Point out each leukocyte.
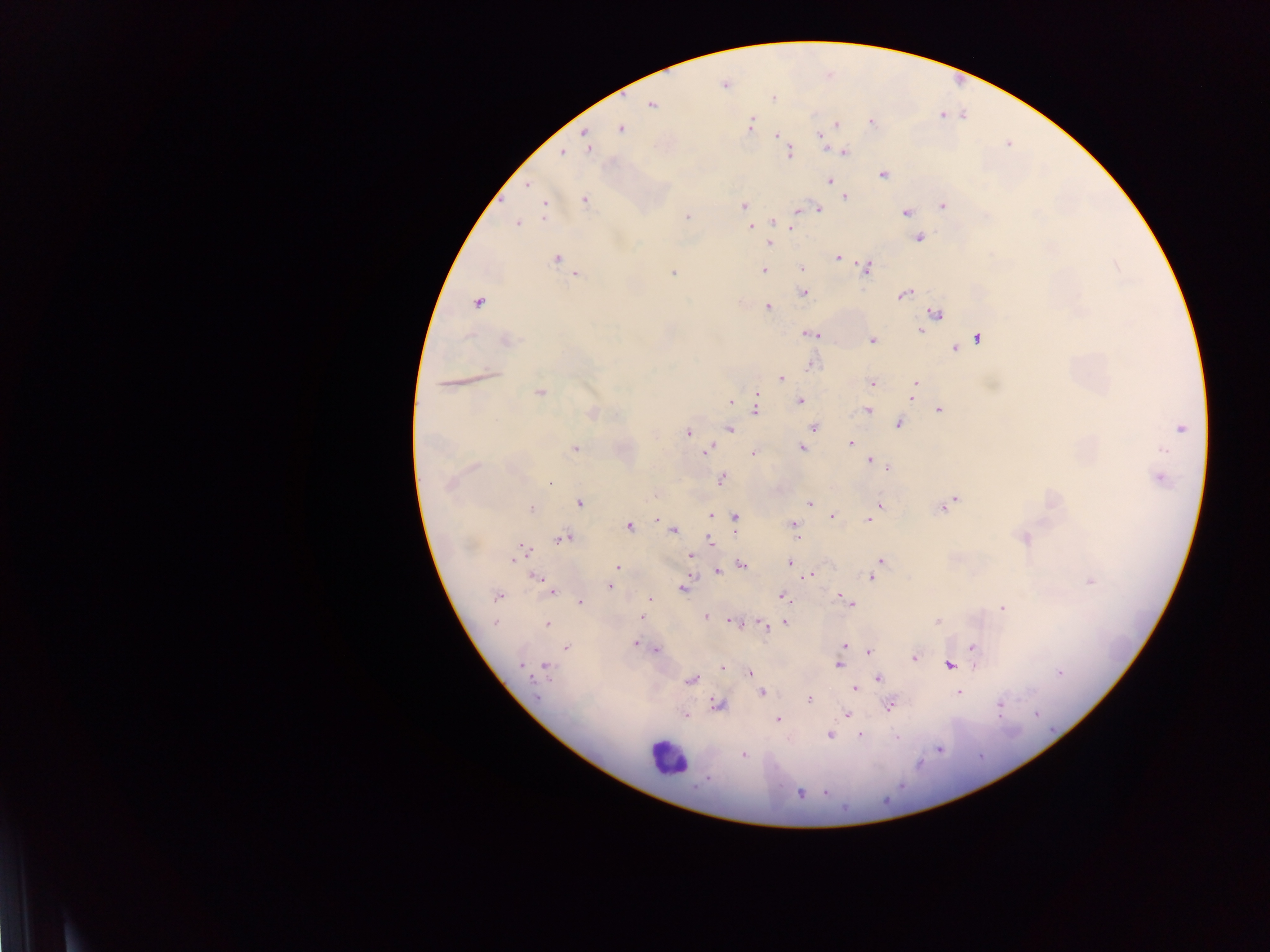

Approximate centers as {x, y} in pixels.
Leukocytes: {666, 758}.

Summary:
  - Malaria parasite locations: {725, 85}, {772, 98}, {651, 105}, {941, 115}, {871, 121}, {750, 125}, {836, 125}, {621, 128}, {777, 135}, {820, 135}, {585, 138}, {589, 147}, {562, 152}, {844, 152}, {789, 153}, {884, 175}, {829, 181}, {527, 185}, {845, 197}, {585, 200}, {744, 205}, {943, 206}, {544, 208}, {800, 209}, {818, 209}, {905, 212}, {687, 216}, {773, 221}, {517, 223}, {790, 226}, {750, 228}, {919, 238}, {769, 244}, {838, 257}, {557, 259}, {868, 268}, {801, 269}, {764, 270}, {673, 272}, {577, 274}, {804, 292}, {904, 295}, {478, 303}, {768, 307}, {936, 313}, {921, 331}, {810, 333}, {978, 338}, {873, 340}, {507, 341}, {956, 348}, {811, 365}, {780, 378}, {872, 383}, {915, 384}, {540, 393}, {912, 397}, {757, 398}, {800, 401}, {731, 403}, {756, 409}, {868, 410}, {940, 411}, {592, 413}, {899, 424}, {813, 428}, {730, 429}, {1180, 429}, {688, 433}, {850, 443}, {802, 447}, {575, 449}, {707, 450}, {753, 453}, {870, 460}, {474, 466}, {888, 468}, {1160, 477}, {722, 479}, {549, 482}, {450, 484}, {952, 501}, {580, 503}, {811, 503}, {880, 505}, {944, 506}, {531, 509}, {710, 516}, {832, 516}, {734, 517}, {868, 520}, {794, 525}, {629, 527}, {673, 531}, {563, 538}, {1024, 540}, {711, 541}, {523, 551}, {691, 556}, {880, 561}, {789, 563}, {742, 564}, {617, 568}, {717, 572}, {809, 576}, {871, 577}, {537, 579}, {612, 581}, {1091, 581}, {609, 586}, {684, 588}, {550, 590}, {497, 596}, {782, 597}, {650, 599}, {580, 602}, {847, 602}, {1003, 608}, {640, 617}, {706, 617}, {733, 621}, {937, 621}, {495, 623}, {784, 623}, {547, 625}, {764, 626}, {636, 644}, {845, 645}, {974, 647}, {567, 648}, {655, 650}, {869, 651}, {914, 658}, {521, 664}, {838, 665}, {950, 665}, {723, 666}, {547, 668}, {749, 673}, {1060, 673}, {878, 678}, {691, 680}, {854, 688}, {958, 692}, {763, 693}, {809, 699}, {718, 704}, {889, 705}, {999, 705}, {847, 714}, {1036, 714}, {684, 715}, {778, 720}, {829, 735}, {860, 736}, {939, 749}, {744, 754}, {800, 793}
  - Field of view: single
  - Capture: mobile-phone photograph through a microscope
  - Preparation: thick blood film
  - Image size: 1270×952 pixels
  - Country: Ghana